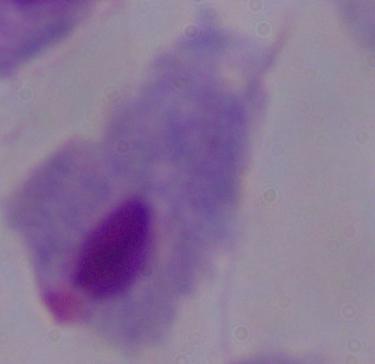
magnification = 1000x
modality = micrograph
identification = trichomonad